State which parasite is depicted.
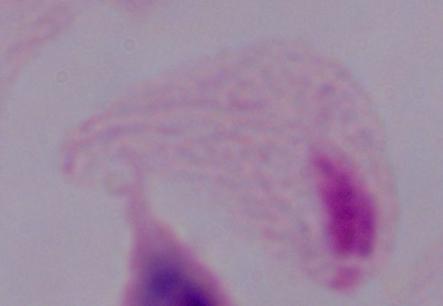
This is a trichomonad.

magnification: 1000x
modality: micrograph